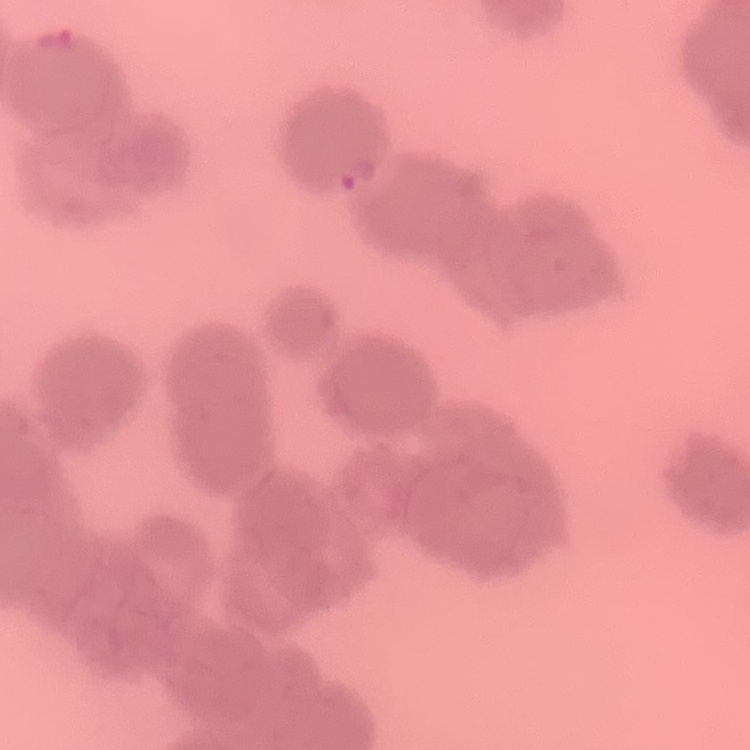
Summary:
  - Erythrocyte morphology: rouleaux formation
  - Image type: one tile cut from a larger photomicrograph
  - Stain: Field's or Giemsa
  - Preparation: thin blood smear